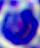

Summary:
  - Magnification: 400x
  - Identification: leukocyte
  - Modality: micrograph